Give the extent of all Plasmodium falciparum-infected red blood cells.
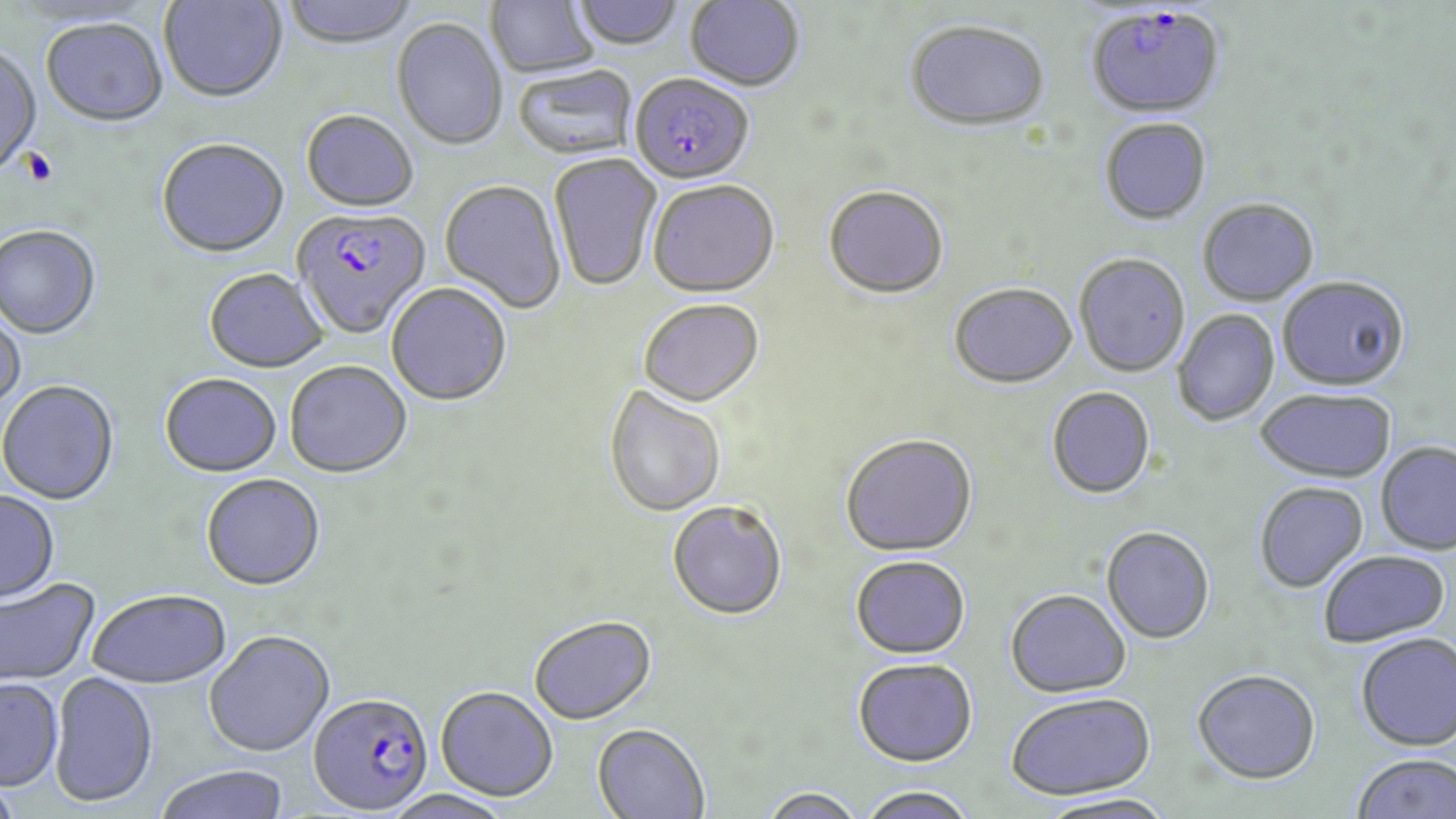

Approximate bounding boxes as (x1, y1, x2, y2) in pixels.
Plasmodium falciparum-infected red blood cells: (1086, 8, 1227, 121), (630, 76, 753, 187), (292, 209, 431, 341), (307, 694, 435, 816).

slide-level diagnosis = Plasmodium falciparum
stain = May-Grünwald-Giemsa
uninfected red blood cell locations = approximate bounding boxes as (x1, y1, x2, y2) in pixels: (159, 0, 287, 105), (281, 0, 421, 50), (486, 0, 600, 79), (572, 0, 684, 52), (685, 1, 805, 92), (392, 19, 508, 152), (40, 20, 169, 130), (904, 22, 1050, 134), (0, 46, 43, 182), (513, 67, 639, 162), (301, 112, 419, 214), (1099, 119, 1212, 227), (156, 139, 290, 260), (548, 154, 662, 294), (439, 180, 566, 315), (647, 182, 781, 301), (823, 188, 949, 302), (1198, 200, 1319, 307), (0, 227, 101, 340), (1074, 256, 1191, 378), (204, 270, 329, 375), (1277, 277, 1410, 393), (386, 284, 512, 409), (948, 285, 1078, 391), (639, 301, 764, 409), (0, 308, 27, 416), (1173, 309, 1280, 426), (285, 363, 411, 481), (159, 375, 282, 479), (0, 382, 119, 507), (603, 387, 726, 518), (1046, 387, 1156, 500), (1256, 390, 1396, 483), (840, 436, 978, 559), (1375, 441, 1456, 555), (200, 475, 325, 593), (1254, 482, 1368, 593), (0, 491, 60, 606), (666, 502, 787, 623), (1101, 526, 1215, 645), (1317, 550, 1451, 648), (850, 557, 971, 661), (0, 578, 101, 690), (87, 590, 231, 691), (1005, 590, 1131, 699), (529, 617, 657, 727), (203, 632, 335, 759), (1355, 632, 1456, 751), (853, 659, 978, 768), (1192, 669, 1321, 784), (50, 672, 158, 809), (0, 678, 63, 792), (435, 688, 558, 803), (1006, 693, 1155, 801), (591, 725, 710, 819), (1350, 753, 1456, 819), (152, 765, 292, 819), (0, 769, 23, 819), (857, 787, 977, 819), (759, 788, 866, 819), (383, 791, 515, 819), (1038, 794, 1177, 819)
magnification = 1000x
preparation = thin blood film
image size = 1456×819 pixels
field of view = single
modality = optical microscopy